Locate and identify every blood parasite.
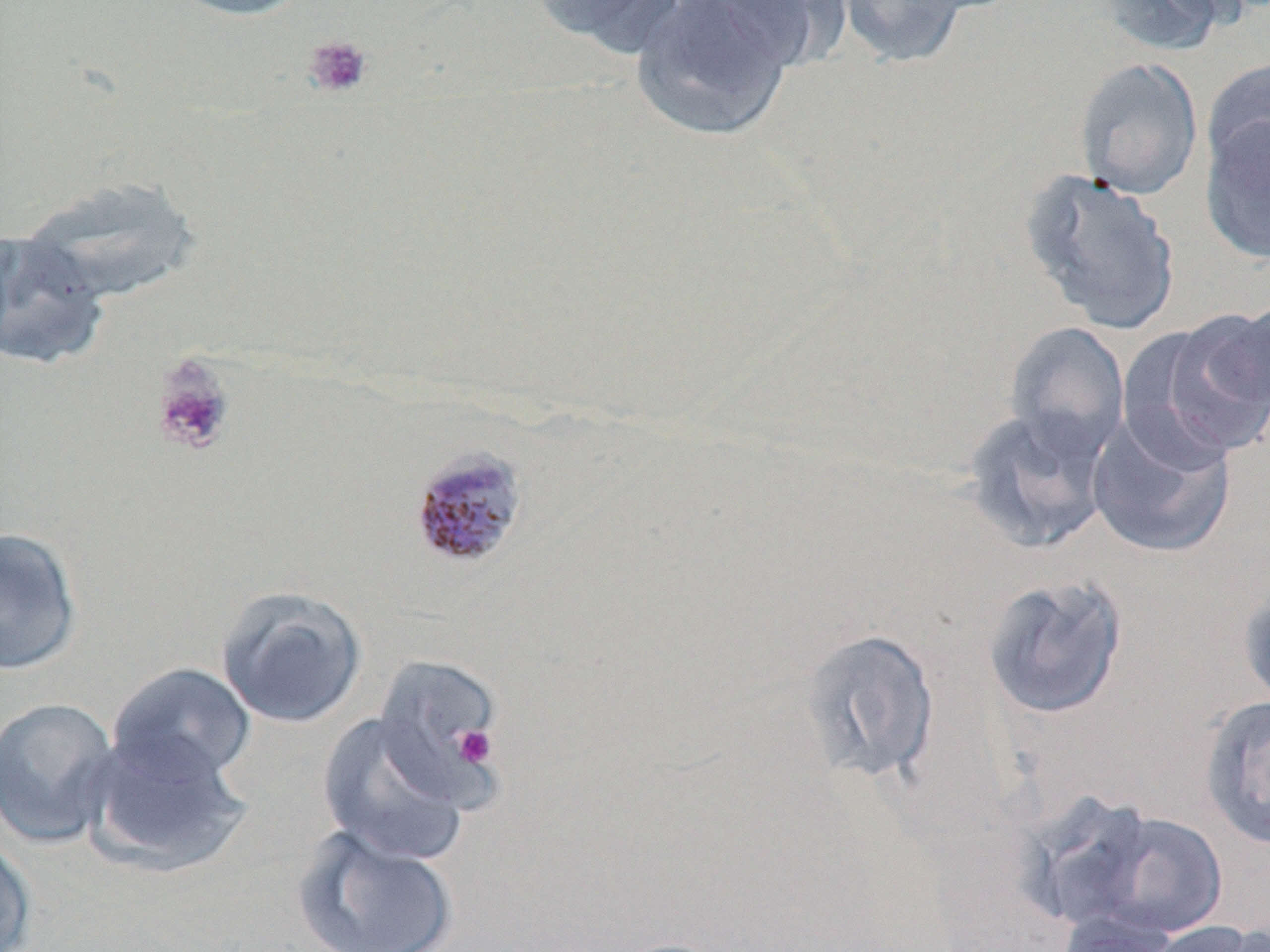
Approximate bounding boxes as (x1, y1, x2, y2) in pixels.
Plasmodium malariae-infected red blood cells: (406, 443, 530, 572).
No Plasmodium falciparum, Plasmodium ovale, Plasmodium vivax, Babesia divergens, or Trypanosoma brucei observed.

Uninfected red blood cell locations: (164, 0, 315, 21), (529, 0, 690, 56), (629, 0, 794, 142), (693, 0, 846, 73), (835, 0, 974, 70), (1096, 0, 1238, 57), (1073, 56, 1203, 201), (1202, 58, 1270, 180), (1199, 114, 1270, 265), (1019, 167, 1183, 334), (18, 176, 203, 304), (0, 229, 112, 371), (1228, 298, 1270, 416), (1130, 311, 1270, 462), (1004, 321, 1130, 458), (961, 405, 1114, 554), (1086, 411, 1236, 560), (0, 525, 84, 677), (981, 573, 1130, 721), (1237, 580, 1270, 711), (215, 584, 368, 729), (795, 627, 942, 787), (373, 653, 506, 807), (106, 662, 257, 788), (1199, 694, 1270, 852), (0, 696, 122, 849), (316, 712, 470, 867), (81, 730, 252, 880), (1066, 806, 1229, 943), (291, 825, 460, 952), (0, 832, 37, 952), (1056, 910, 1181, 952), (1142, 919, 1267, 952), (606, 936, 740, 952). Platelet locations: (303, 35, 373, 99), (150, 354, 237, 455), (452, 725, 496, 767). Slide-level diagnosis: Plasmodium malariae. Light microscopy. Image is 1270×952 pixels. Captured at 1000x magnification. One field of a larger specimen. Thin blood film. May-Grünwald-Giemsa-stained preparation.